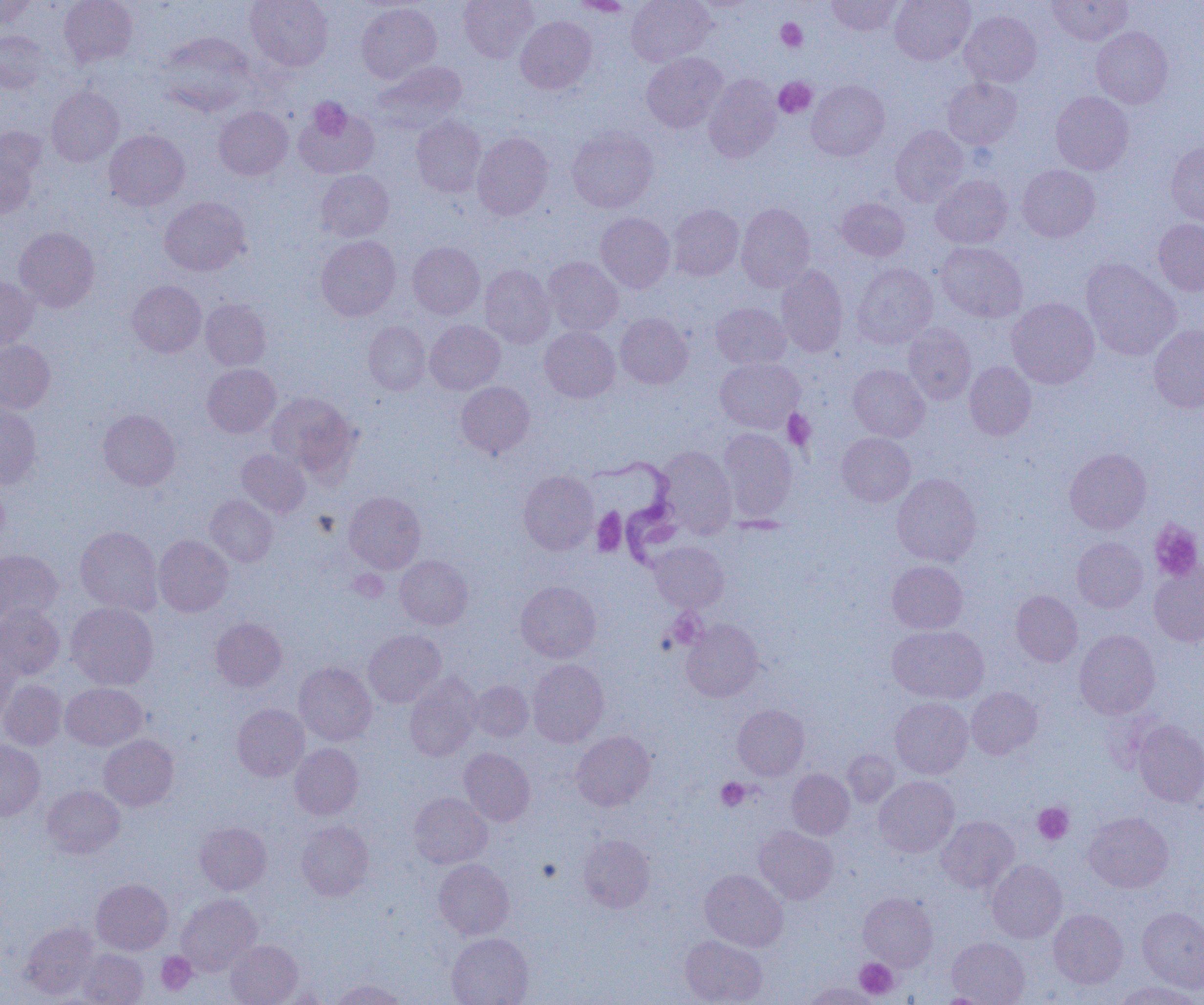
Approximate bounding boxes as (x1,y1)-(x2,y2) corner pairs in pixels. Platelet locations: (776,19)-(807,51), (773,77)-(816,118), (309,98)-(352,140), (782,410)-(815,450), (592,508)-(627,557), (1149,520)-(1203,582), (348,569)-(388,602), (716,778)-(750,811), (1033,803)-(1073,844), (537,858)-(562,882), (157,952)-(197,995), (855,958)-(898,999). Trypanosoma brucei locations: (589,455)-(684,569). Uninfected red blood cell locations: (59,0)-(138,67), (246,0)-(333,71), (459,0)-(538,62), (569,0)-(635,14), (626,0)-(716,67), (826,0)-(902,36), (890,0)-(975,65), (1046,0)-(1132,46), (0,1)-(35,30), (356,3)-(441,83), (960,11)-(1042,87), (515,16)-(596,94), (1091,26)-(1173,108), (0,31)-(50,94), (156,32)-(257,116), (641,52)-(728,133), (371,61)-(466,133), (704,74)-(781,162), (942,77)-(1022,149), (807,80)-(890,161), (46,86)-(124,166), (1051,91)-(1133,174), (293,102)-(379,180), (214,107)-(292,180), (411,115)-(486,198), (890,125)-(969,207), (567,127)-(658,213), (104,130)-(190,210), (0,132)-(43,219), (472,132)-(554,220), (1166,140)-(1204,226), (1017,165)-(1100,242), (316,170)-(394,241), (930,175)-(1012,249), (160,197)-(250,276), (836,198)-(910,261), (736,203)-(815,291), (668,204)-(743,281), (595,213)-(675,292), (1153,219)-(1204,295), (14,227)-(99,312), (316,235)-(400,321), (408,242)-(484,319), (935,242)-(1027,322), (543,257)-(623,335), (1080,258)-(1180,360), (852,263)-(937,349), (480,264)-(556,348), (776,264)-(848,357), (0,276)-(38,349), (127,280)-(206,357), (1007,298)-(1099,389), (200,299)-(271,371), (711,303)-(791,369), (616,313)-(693,388), (425,320)-(505,395), (363,321)-(430,395), (903,324)-(976,404), (1148,325)-(1204,412), (539,326)-(620,402), (0,340)-(55,414), (715,358)-(804,432), (965,361)-(1036,440), (202,364)-(280,438), (848,364)-(929,441), (456,381)-(534,459), (266,392)-(360,481), (0,403)-(41,489), (98,409)-(180,490), (718,428)-(797,523), (837,433)-(915,506), (657,447)-(736,537), (236,448)-(310,518), (1064,448)-(1151,534), (519,471)-(599,555), (892,473)-(982,566), (0,479)-(9,551), (344,491)-(425,573), (205,495)-(278,566), (75,526)-(163,616), (154,535)-(233,617), (1072,537)-(1148,612), (650,542)-(729,612), (0,549)-(62,624), (395,555)-(473,629), (887,561)-(968,634), (1149,562)-(1204,647), (515,581)-(601,662), (1011,590)-(1082,667), (66,602)-(158,690), (0,605)-(65,679), (211,618)-(287,692), (681,619)-(763,702), (888,626)-(988,703), (363,629)-(446,707), (1074,630)-(1160,719), (0,644)-(20,724), (528,659)-(609,747), (294,661)-(377,746), (404,673)-(481,761), (0,679)-(66,750), (470,681)-(533,742), (61,683)-(147,751), (966,687)-(1042,759), (891,697)-(973,778), (232,704)-(309,781), (732,704)-(809,780), (1133,720)-(1204,807), (571,730)-(655,811), (99,735)-(179,811), (0,740)-(45,820), (290,743)-(363,819), (459,748)-(535,825), (843,750)-(898,807), (787,769)-(854,839), (875,776)-(959,857), (42,785)-(125,858), (409,793)-(492,868), (1083,812)-(1173,892), (936,816)-(1019,893), (296,820)-(374,900), (195,822)-(271,894), (754,826)-(839,904), (577,834)-(655,912), (434,859)-(514,939), (987,860)-(1066,943), (700,869)-(788,951), (92,878)-(173,955), (858,892)-(937,970), (176,893)-(262,976), (1137,907)-(1204,993), (1049,909)-(1128,988), (20,922)-(99,999), (447,933)-(533,1005), (680,934)-(767,1005), (947,937)-(1030,1004), (225,940)-(302,1005), (78,949)-(149,1005), (331,979)-(407,1005), (1112,981)-(1203,1005), (801,982)-(880,1005), (933,993)-(1000,1004). Slide-level diagnosis: Trypanosoma brucei. Captured at 1000x magnification. One field of a larger specimen. Image is 1204×1005 pixels. Light microscopy. Thin blood film.